State the blood parasite species.
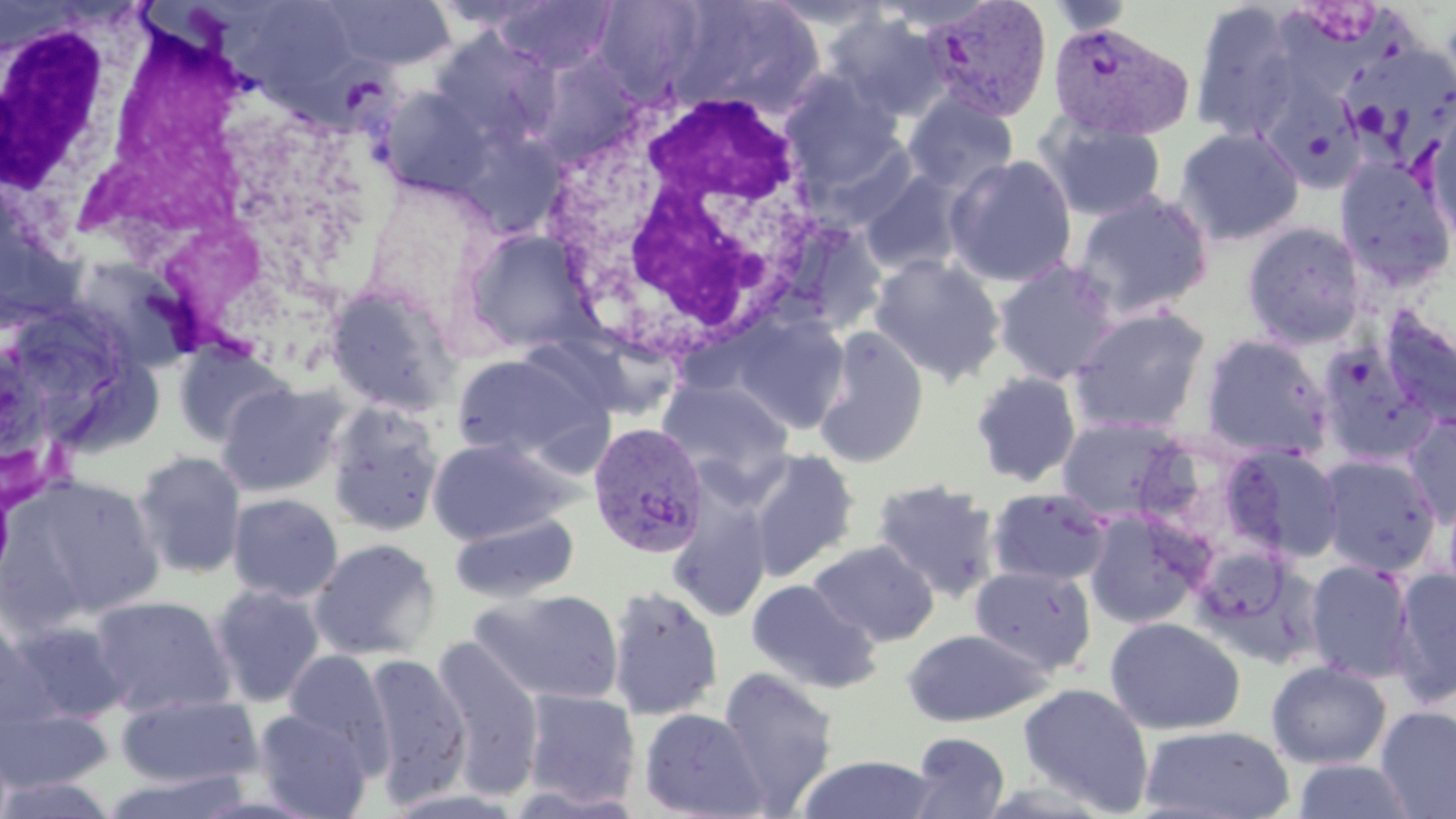

Plasmodium vivax.

Summary:
  - Coordinate format: approximate bounding boxes as (x1,y1)-(x2,y2) corner pairs in pixels
  - Plasmodium vivax-infected red blood cell locations: (924,0)-(1052,121), (1048,21)-(1194,142), (587,421)-(709,559)
  - Uninfected red blood cell locations: (321,0)-(456,70), (491,1)-(617,73), (591,1)-(711,100), (660,1)-(828,118), (1045,1)-(1137,36), (1189,1)-(1306,142), (828,12)-(950,122), (1341,41)-(1456,156), (531,54)-(640,164), (779,73)-(907,193), (1258,77)-(1368,193), (376,84)-(498,199), (904,92)-(1018,195), (1421,103)-(1456,251), (1045,120)-(1166,221), (1174,127)-(1304,246), (945,155)-(1077,287), (1333,156)-(1455,291), (861,171)-(966,276), (1072,189)-(1213,320), (1242,222)-(1368,349), (463,227)-(593,353), (869,255)-(1006,386), (993,259)-(1121,385), (325,282)-(460,416), (1070,306)-(1212,433), (1379,306)-(1456,428), (726,311)-(851,434), (813,326)-(929,469), (1199,333)-(1333,460), (1315,341)-(1440,467), (173,342)-(290,448), (451,352)-(608,465), (969,370)-(1082,487), (657,377)-(794,491), (217,382)-(347,498), (325,402)-(445,537), (1403,412)-(1455,527), (1057,416)-(1188,522), (427,437)-(570,544), (1222,442)-(1346,563), (745,448)-(860,580), (132,449)-(247,579), (1318,454)-(1440,576), (9,473)-(166,624), (872,478)-(1001,602), (985,487)-(1112,587), (227,493)-(344,603), (669,500)-(772,622), (1082,508)-(1211,629), (450,512)-(579,604), (309,538)-(441,661), (808,539)-(939,647), (1304,559)-(1416,683), (969,564)-(1096,675), (1390,565)-(1456,706), (746,578)-(880,693), (207,585)-(325,707), (606,585)-(723,720), (472,588)-(624,706), (89,594)-(236,717), (0,614)-(48,731), (1105,617)-(1246,736), (8,619)-(134,724), (902,628)-(1052,727), (430,636)-(546,800), (281,649)-(394,771), (361,651)-(471,806), (1266,659)-(1392,770), (716,667)-(839,812), (1017,682)-(1154,814), (520,689)-(641,809), (116,692)-(262,789), (1375,706)-(1456,818), (0,707)-(112,793), (637,707)-(769,819), (251,708)-(373,818), (1139,724)-(1296,819), (906,732)-(1011,819), (796,754)-(939,818), (1289,758)-(1422,818), (97,770)-(252,818), (0,775)-(121,819)
  - White blood cell locations: (113,2)-(319,368), (0,8)-(144,249), (538,78)-(837,370)
  - Stain: May-Grünwald-Giemsa
  - Modality: optical microscopy
  - Preparation: thin blood smear
  - Magnification: 1000x
  - Image size: 1456×819 pixels
  - Field of view: one of a larger specimen